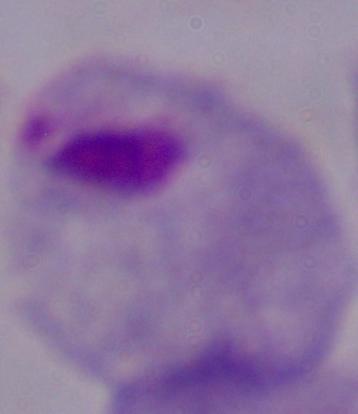

A trichomonad is seen. Micrograph. Captured at 1000x magnification.